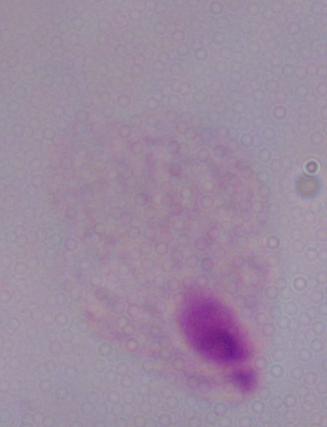

Micrograph. Captured at 1000x magnification. A trichomonad is shown.